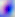
identification: Toxoplasma gondii
magnification: 400x
modality: micrograph